Identify the parasite.
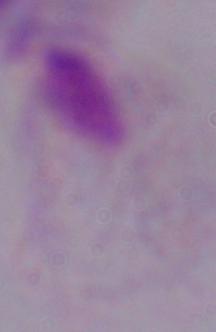
A trichomonad.

Summary:
  - Modality: micrograph
  - Magnification: 1000x